Outline each blood parasite and name the species.
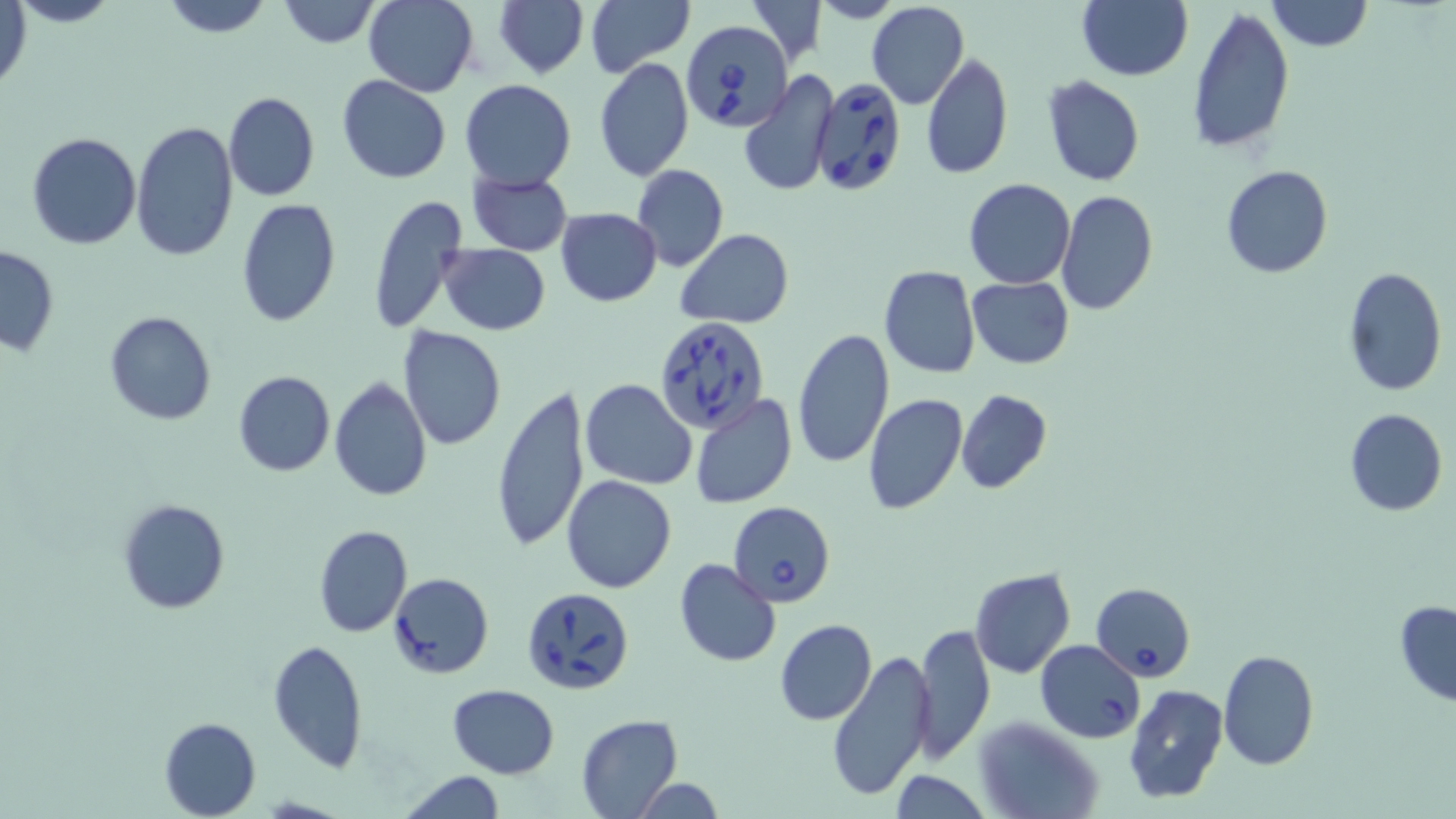

Approximate bounding boxes as (x1, y1, x2, y2) in pixels.
Babesia divergens-infected red blood cells: (681, 19, 791, 133), (808, 76, 908, 198), (653, 317, 771, 434), (729, 501, 836, 606), (1091, 582, 1195, 680), (520, 587, 634, 697), (1034, 639, 1145, 742).
No Plasmodium falciparum, Plasmodium ovale, Plasmodium malariae, Plasmodium vivax, or Trypanosoma brucei observed.

{
  "slide_level_diagnosis": "Babesia divergens",
  "stain": "May-Grünwald-Giemsa",
  "preparation": "thin blood smear",
  "magnification": "1000x",
  "uninfected_red_blood_cell_locations": "approximate bounding boxes as (x1, y1, x2, y2) in pixels: (160, 0, 274, 38), (278, 0, 381, 47), (494, 0, 587, 79), (586, 0, 694, 79), (746, 0, 828, 65), (1077, 0, 1193, 81), (1267, 0, 1373, 53), (364, 1, 479, 97), (866, 1, 969, 110), (0, 2, 33, 98), (1189, 5, 1294, 155), (921, 52, 1013, 179), (593, 58, 694, 183), (737, 72, 838, 195), (337, 75, 452, 183), (1042, 75, 1145, 187), (459, 78, 577, 190), (223, 91, 320, 202), (130, 121, 238, 262), (25, 132, 141, 249), (631, 163, 728, 272), (1221, 165, 1333, 279), (467, 170, 572, 256), (964, 177, 1074, 289), (1056, 190, 1158, 315), (368, 194, 470, 334), (236, 198, 342, 328), (556, 207, 661, 307), (676, 230, 794, 327), (437, 243, 551, 335), (0, 245, 58, 354), (878, 265, 981, 379), (1342, 266, 1447, 396), (967, 276, 1073, 369), (811, 283, 934, 436), (104, 311, 216, 425), (396, 325, 508, 451), (792, 327, 895, 469), (232, 372, 336, 477), (328, 377, 433, 502), (580, 379, 697, 489), (490, 386, 590, 554), (956, 389, 1052, 494), (863, 393, 969, 515), (688, 394, 797, 509), (1344, 409, 1446, 517), (561, 475, 677, 593), (118, 497, 231, 616), (313, 524, 412, 637), (674, 559, 781, 667), (970, 568, 1076, 679), (389, 572, 494, 678), (1394, 599, 1456, 705), (775, 619, 877, 724), (913, 622, 995, 764), (268, 639, 369, 771), (1218, 648, 1319, 770), (826, 650, 937, 801), (1122, 684, 1229, 804), (447, 685, 560, 778), (575, 714, 683, 817), (975, 715, 1103, 819), (158, 717, 260, 818), (394, 770, 511, 819), (629, 777, 726, 818)",
  "modality": "light microscopy",
  "image_size": "1456×819 pixels",
  "field_of_view": "one of a larger specimen"
}